Assess the morphology of the erythrocytes.
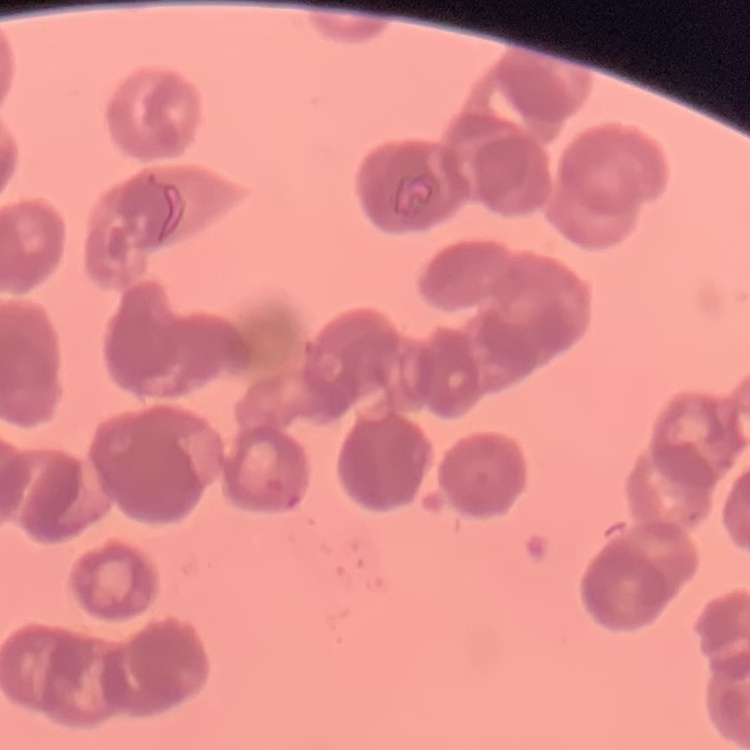

They show rouleaux formation.

preparation = thin blood film
image type = one tile cut from a larger photomicrograph
stain = Field's or Giemsa